Locate platelets.
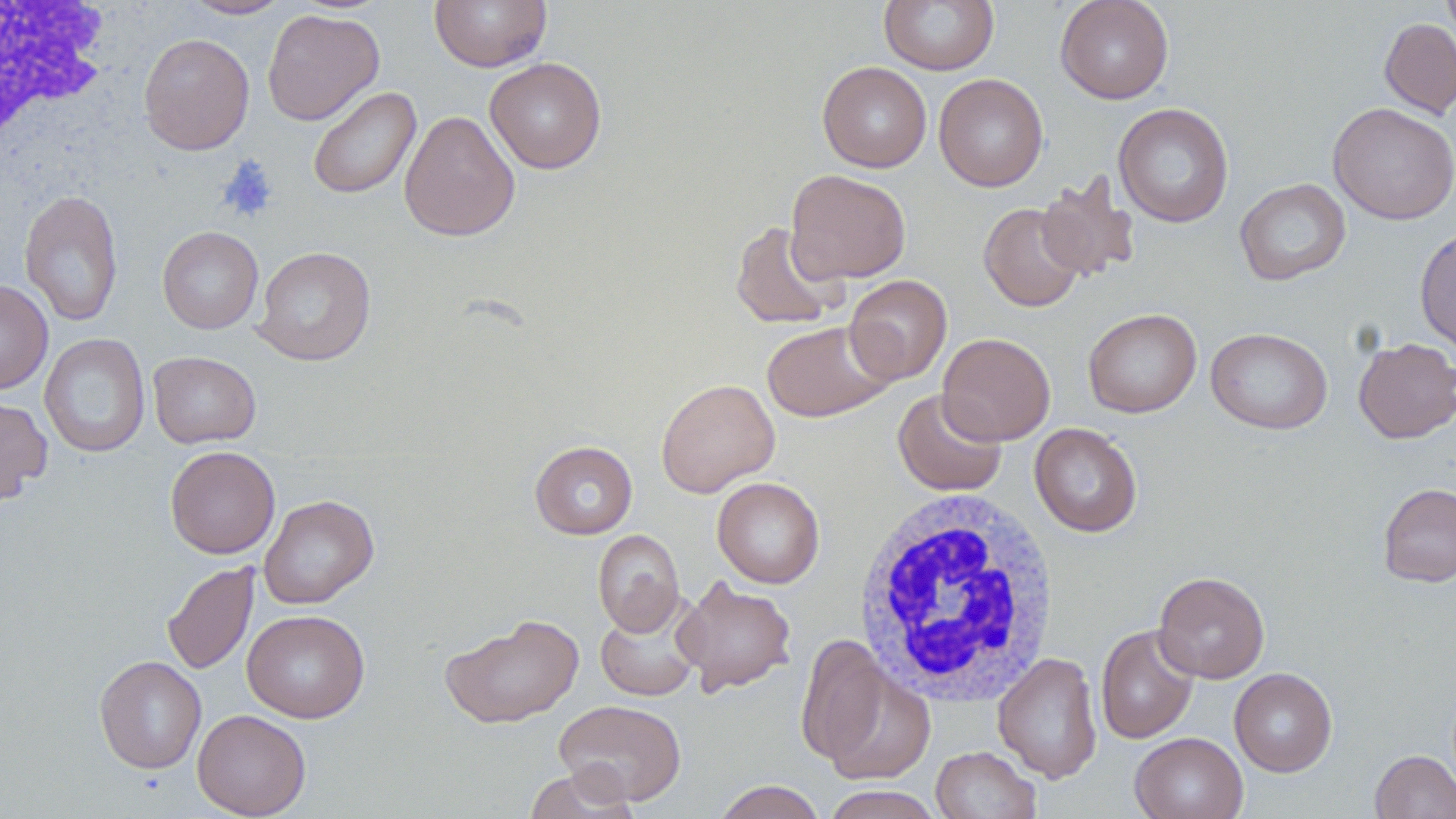

Approximate bounding boxes as [x1, y1, x2, y2] in pixels.
Platelets: [216, 156, 279, 223].

Uninfected red blood cell locations: [184, 0, 292, 19], [430, 0, 551, 71], [1055, 0, 1174, 104], [1440, 0, 1456, 46], [879, 1, 999, 74], [262, 9, 384, 126], [1379, 18, 1456, 119], [138, 33, 255, 154], [485, 57, 607, 174], [817, 61, 932, 173], [934, 73, 1048, 192], [307, 86, 421, 199], [1327, 102, 1456, 225], [1113, 103, 1234, 228], [399, 110, 520, 242], [785, 169, 911, 284], [1036, 175, 1141, 282], [1234, 178, 1351, 286], [19, 189, 123, 326], [979, 203, 1086, 312], [728, 220, 847, 330], [1415, 225, 1455, 356], [157, 226, 264, 334], [252, 246, 376, 366], [844, 275, 952, 385], [0, 279, 53, 395], [1082, 308, 1202, 418], [762, 320, 894, 422], [1206, 327, 1332, 434], [39, 332, 150, 458], [937, 332, 1056, 445], [1353, 337, 1456, 444], [148, 351, 261, 448], [656, 378, 780, 497], [892, 388, 1007, 496], [0, 396, 53, 505], [1029, 424, 1142, 537], [529, 440, 638, 539], [165, 445, 280, 559], [712, 476, 825, 588], [1377, 483, 1456, 587], [259, 494, 379, 609], [593, 529, 685, 636], [162, 561, 258, 674], [1153, 571, 1270, 683], [673, 576, 797, 696], [595, 592, 706, 702], [241, 609, 370, 723], [440, 614, 584, 728], [1095, 623, 1199, 744], [796, 634, 892, 769], [992, 652, 1103, 783], [94, 655, 207, 773], [821, 665, 935, 784], [1229, 667, 1337, 777], [554, 699, 687, 806], [192, 709, 311, 818], [1130, 732, 1248, 819], [930, 746, 1041, 819], [1370, 749, 1456, 819], [523, 766, 640, 819], [712, 780, 826, 819], [820, 785, 944, 818]. White blood cell locations: [0, 3, 116, 166], [853, 488, 1062, 705]. Slide-level diagnosis: no evidence of blood parasites. One field of a larger specimen. Thin blood film. Image is 1456×819 pixels. Captured at 1000x magnification. Light microscopy. May-Grünwald-Giemsa-stained preparation.